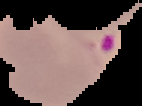
Image is 142×106 pixels. From a thin blood smear. Result: malaria parasites detected. Cell region segmented out of the field of view; the surrounding area is masked to black.